Name the parasite shown.
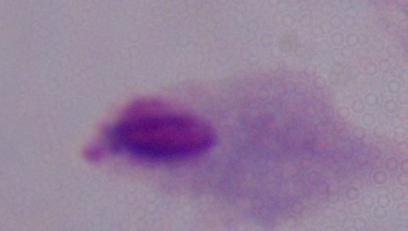

This is a trichomonad.

magnification = 1000x
modality = micrograph